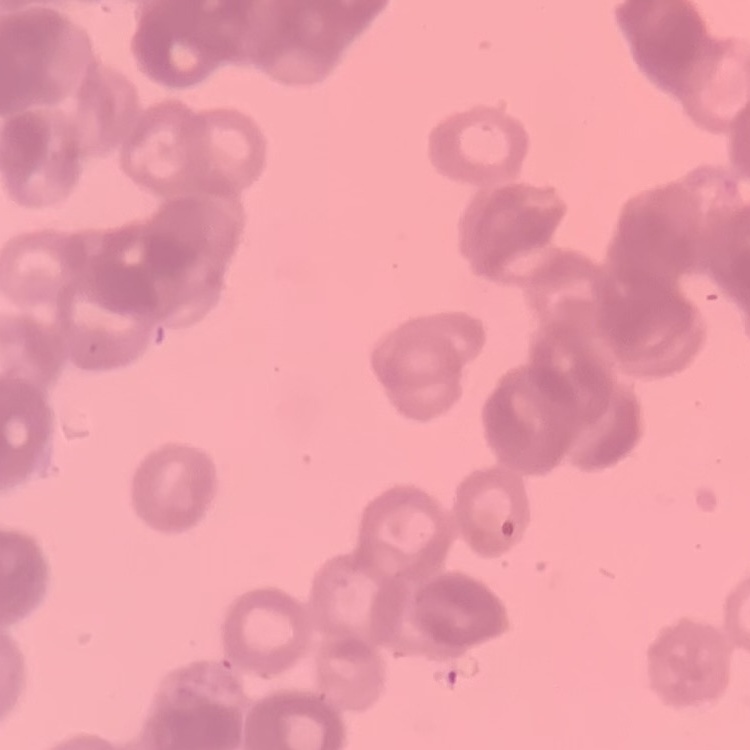
Summary:
  - Red blood cell morphology: rouleaux formation
  - Preparation: thin blood smear
  - Stain: Field's or Giemsa
  - Image type: square crop of a larger photomicrograph